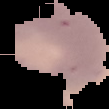
Summary:
  - Preparation: thin blood smear
  - Image type: segmented cell region on a black background
  - Image size: 109×109 pixels
  - Malaria status: uninfected